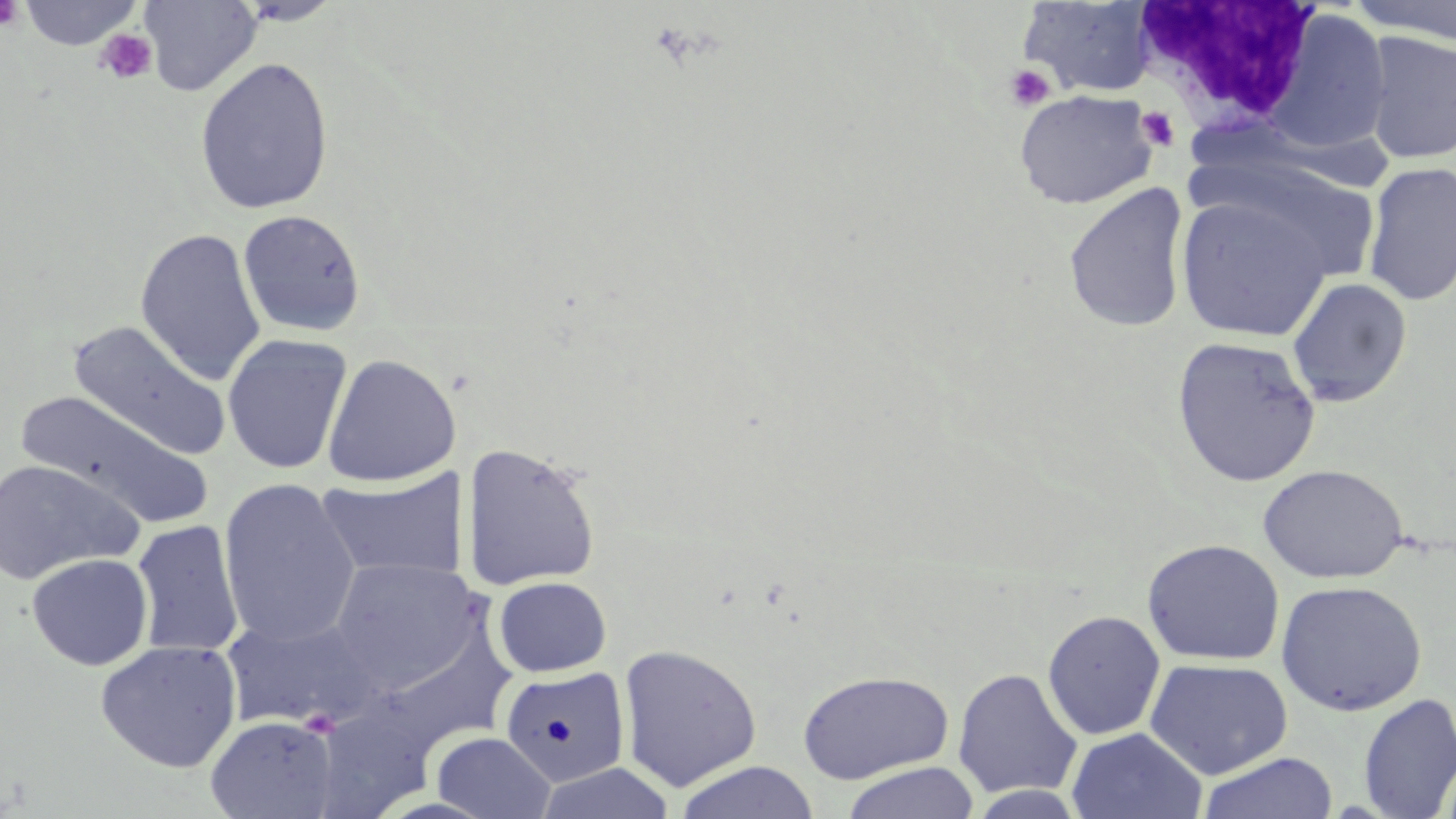
slide_level_diagnosis: no evidence of blood parasites
stain: May-Grünwald-Giemsa
preparation: thin blood smear
field_of_view: single
modality: light microscopy
platelet_locations: 'approximate bounding boxes as (x1,y1)-(x2,y2) corner pairs in pixels: (0,0)-(25,32), (95,29)-(159,85), (1003,63)-(1055,112), (1135,106)-(1181,151)'
magnification: 1000x
white_blood_cell_locations: 'approximate bounding boxes as (x1,y1)-(x2,y2) corner pairs in pixels: (1131,3)-(1323,135)'
image_size: 1456×819 pixels
uninfected_red_blood_cell_locations: 'approximate bounding boxes as (x1,y1)-(x2,y2) corner pairs in pixels: (16,0)-(145,50), (140,1)-(262,96), (1018,1)-(1158,98), (1348,1)-(1456,44), (1265,7)-(1394,157), (1359,31)-(1456,165), (194,56)-(334,216), (1014,89)-(1158,209), (1185,148)-(1390,293), (1362,161)-(1456,306), (1062,183)-(1191,334), (1175,195)-(1333,342), (237,208)-(367,338), (134,227)-(267,386), (1286,277)-(1412,407), (67,321)-(230,459), (221,333)-(352,475), (1171,336)-(1322,488), (322,353)-(460,487), (15,391)-(214,528), (461,441)-(602,591), (0,459)-(143,586), (1258,463)-(1410,583), (317,467)-(468,583), (218,477)-(361,649), (131,520)-(244,657), (1142,538)-(1286,666), (27,552)-(153,670), (329,557)-(488,691), (493,576)-(612,677), (1276,580)-(1427,716), (1042,609)-(1166,741), (221,614)-(385,732), (364,620)-(520,757), (94,639)-(243,772), (616,642)-(763,793), (1144,658)-(1293,780), (500,665)-(631,789), (951,668)-(1083,799), (796,669)-(956,784), (1357,692)-(1456,819), (204,714)-(340,819), (1066,727)-(1207,818), (432,731)-(555,819), (1197,752)-(1339,819), (672,760)-(820,819), (840,761)-(980,819)'